Assess this cell for malaria.
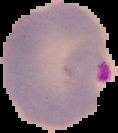

It is parasitized.

Summary:
  - Preparation: thin blood film
  - Image type: cell region segmented out of the field of view; surrounding area masked to black
  - Image size: 118×133 pixels